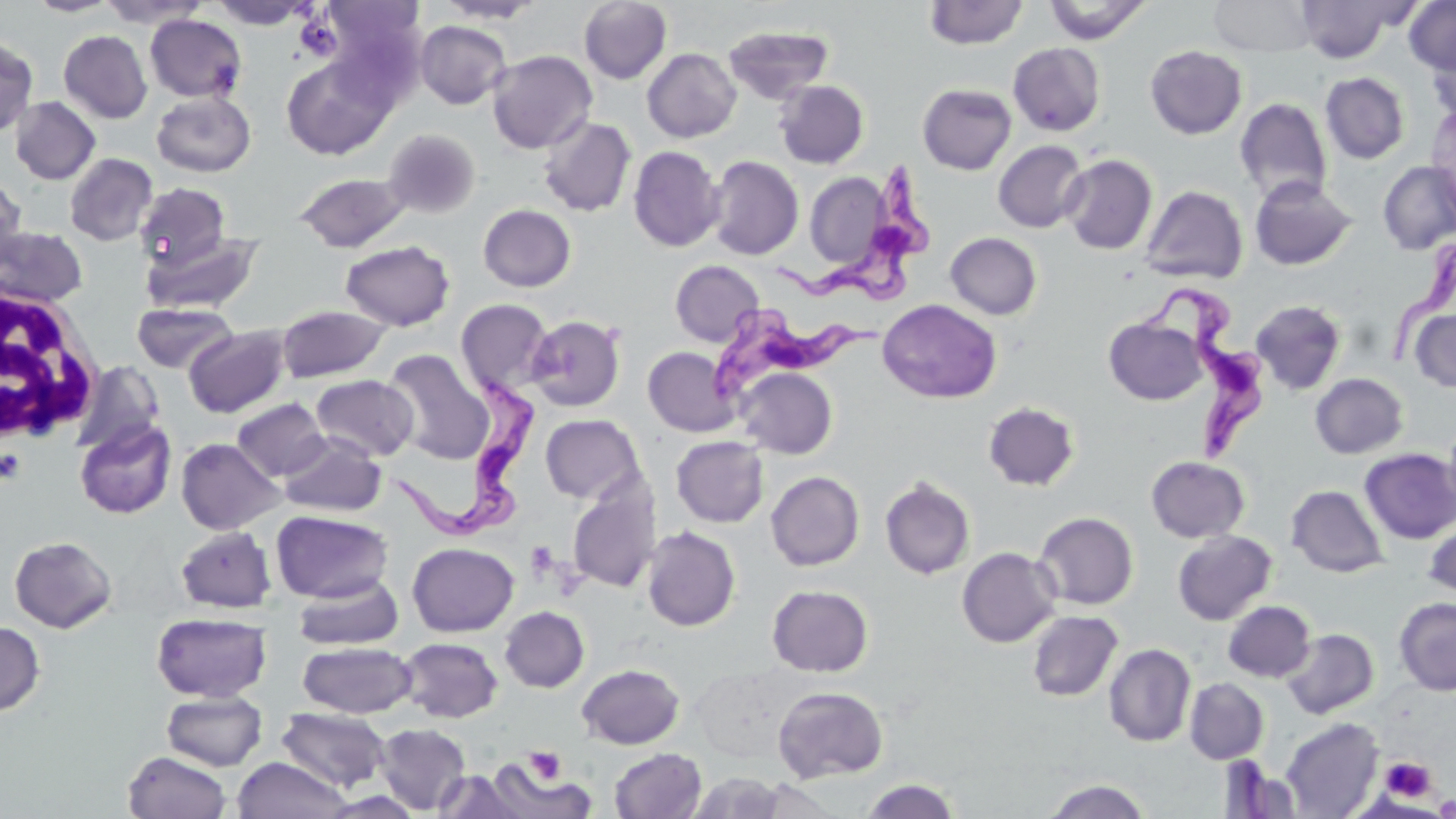

Approximate bounding boxes as (x1,y1)-(x2,y2) corner pairs in pixels. White blood cell locations: (0,285)-(103,448). Uninfected red blood cell locations: (25,0)-(122,17), (98,0)-(209,28), (209,0)-(313,29), (435,0)-(547,24), (578,0)-(673,85), (1043,0)-(1152,45), (1209,0)-(1318,57), (322,1)-(427,87), (923,1)-(1028,49), (1404,1)-(1456,74), (1296,2)-(1402,62), (145,14)-(247,102), (415,20)-(512,109), (722,23)-(834,104), (58,30)-(152,123), (0,35)-(39,137), (1427,37)-(1456,124), (1008,42)-(1106,136), (1144,45)-(1248,139), (642,48)-(741,143), (487,50)-(597,153), (281,54)-(394,160), (1320,72)-(1410,164), (774,79)-(870,169), (917,83)-(1017,175), (151,90)-(256,177), (10,96)-(100,185), (1234,98)-(1332,205), (1426,106)-(1456,225), (538,116)-(636,216), (383,129)-(480,217), (993,140)-(1088,233), (628,145)-(724,252), (64,153)-(157,246), (1060,154)-(1157,255), (707,155)-(804,260), (1377,161)-(1456,255), (804,170)-(891,272), (294,172)-(412,252), (0,174)-(26,271), (1249,175)-(1358,271), (134,182)-(233,271), (1140,184)-(1249,284), (478,204)-(576,292), (0,225)-(89,308), (142,229)-(262,315), (945,232)-(1042,319), (340,239)-(455,331), (669,260)-(764,346), (454,298)-(555,397), (878,299)-(1002,404), (1250,299)-(1347,396), (131,301)-(238,374), (276,304)-(392,383), (1409,310)-(1456,392), (526,314)-(625,412), (1103,317)-(1208,405), (183,325)-(291,418), (643,346)-(740,437), (382,349)-(493,463), (70,361)-(165,456), (735,367)-(838,458), (1310,373)-(1408,458), (310,374)-(419,461), (233,398)-(331,481), (983,401)-(1080,491), (540,414)-(646,504), (75,418)-(177,519), (1443,422)-(1456,518), (278,432)-(387,516), (671,436)-(769,527), (176,438)-(285,534), (1359,448)-(1456,544), (1146,455)-(1250,543), (766,471)-(864,571), (880,477)-(975,580), (567,482)-(660,593), (1286,484)-(1388,577), (271,510)-(393,603), (1033,511)-(1139,610), (1423,521)-(1456,597), (175,526)-(276,613), (641,526)-(741,631), (1172,530)-(1276,625), (9,536)-(117,633), (407,542)-(519,636), (956,547)-(1061,648), (293,575)-(403,650), (767,585)-(873,676), (1394,598)-(1456,695), (1223,600)-(1315,682), (499,606)-(589,692), (1026,610)-(1122,701), (152,613)-(272,702), (0,621)-(45,716), (1282,628)-(1378,719), (397,637)-(503,723), (297,641)-(417,719), (1103,643)-(1196,747), (577,663)-(685,749), (1184,678)-(1268,764), (772,686)-(888,782), (161,691)-(267,770), (276,707)-(391,792), (1280,717)-(1384,818), (374,723)-(472,814), (609,748)-(706,819), (123,750)-(232,819), (232,756)-(353,819), (486,759)-(595,818), (434,770)-(525,818), (688,771)-(788,818), (750,777)-(844,818), (859,778)-(962,819), (1043,779)-(1151,818), (1433,794)-(1456,818). Trypanosoma brucei locations: (768,160)-(933,312), (1385,242)-(1456,372), (1148,289)-(1270,462), (702,304)-(887,411), (390,369)-(544,549). Platelet locations: (296,15)-(341,60), (0,448)-(26,487), (525,540)-(560,581), (523,747)-(567,786), (1380,755)-(1436,802), (1434,795)-(1456,817). Slide-level diagnosis: Trypanosoma brucei. May-Grünwald-Giemsa-stained preparation. Thin blood film. Single field of view. Image is 1456×819 pixels. Captured at 1000x magnification. Light microscopy.